State which parasite is depicted.
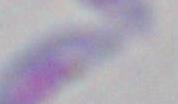
This is Toxoplasma gondii.

1000x magnification. Micrograph.